Name the blood parasite species.
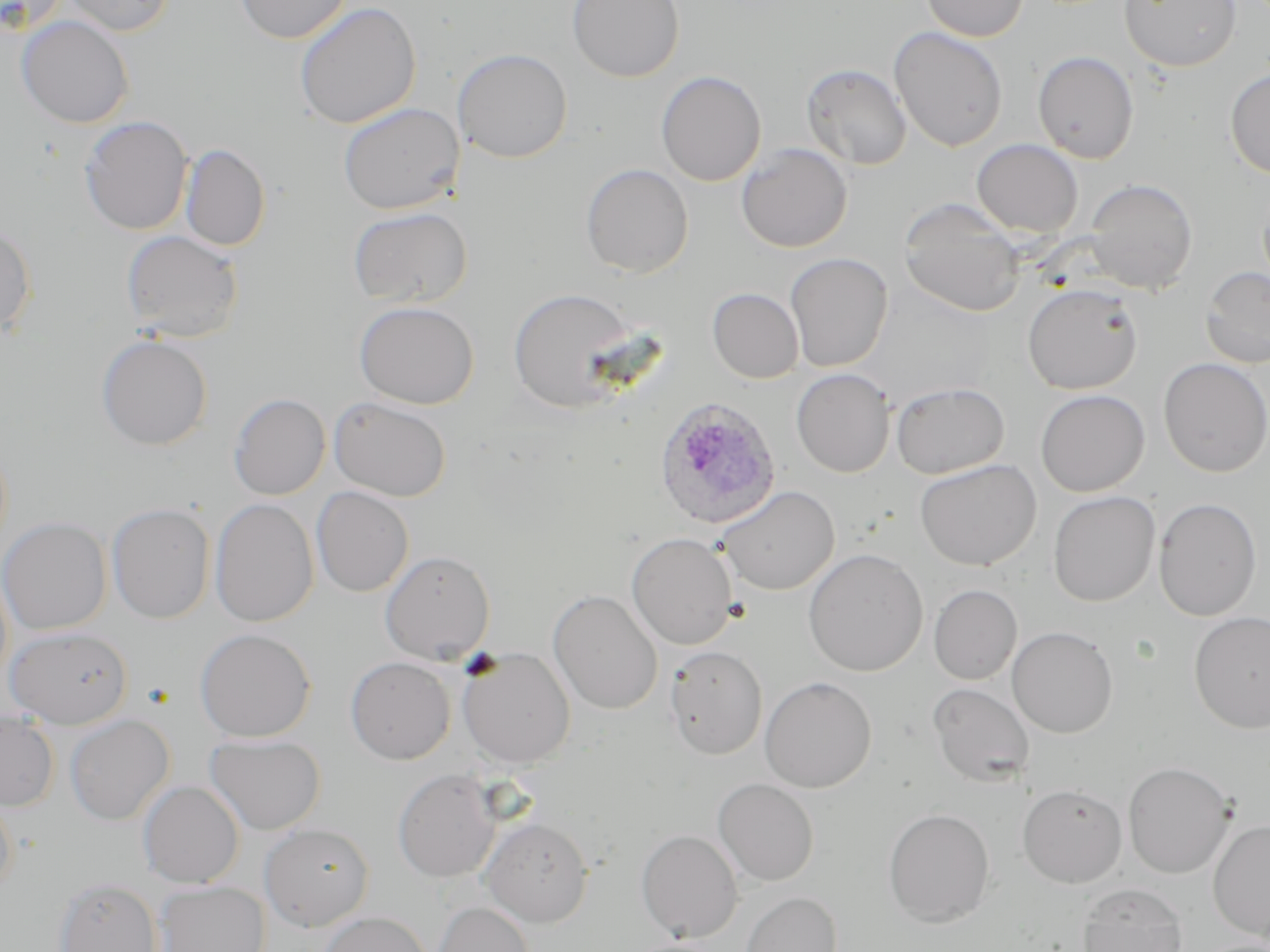

Plasmodium ovale.

Approximate bounding boxes as named x1/y1/x2/y2 corners in pixels. Uninfected red blood cell locations: (x1=3, y1=0, x2=71, y2=35), (x1=60, y1=0, x2=174, y2=36), (x1=234, y1=0, x2=352, y2=44), (x1=567, y1=0, x2=684, y2=82), (x1=921, y1=0, x2=1030, y2=41), (x1=1119, y1=0, x2=1242, y2=72), (x1=294, y1=1, x2=421, y2=130), (x1=16, y1=15, x2=135, y2=129), (x1=889, y1=26, x2=1009, y2=152), (x1=453, y1=48, x2=572, y2=163), (x1=1033, y1=51, x2=1139, y2=164), (x1=801, y1=63, x2=912, y2=171), (x1=1225, y1=68, x2=1270, y2=179), (x1=656, y1=70, x2=766, y2=186), (x1=338, y1=102, x2=462, y2=214), (x1=80, y1=116, x2=193, y2=235), (x1=971, y1=139, x2=1084, y2=238), (x1=736, y1=143, x2=853, y2=253), (x1=180, y1=144, x2=270, y2=251), (x1=580, y1=163, x2=693, y2=278), (x1=1084, y1=178, x2=1198, y2=293), (x1=898, y1=199, x2=1025, y2=316), (x1=348, y1=206, x2=472, y2=308), (x1=0, y1=221, x2=37, y2=336), (x1=121, y1=230, x2=244, y2=343), (x1=785, y1=253, x2=893, y2=372), (x1=1200, y1=266, x2=1270, y2=369), (x1=1022, y1=283, x2=1143, y2=394), (x1=508, y1=288, x2=637, y2=414), (x1=707, y1=288, x2=804, y2=383), (x1=354, y1=300, x2=479, y2=409), (x1=96, y1=335, x2=213, y2=450), (x1=1158, y1=358, x2=1270, y2=477), (x1=791, y1=368, x2=895, y2=477), (x1=890, y1=381, x2=1010, y2=479), (x1=1036, y1=389, x2=1149, y2=496), (x1=229, y1=393, x2=330, y2=500), (x1=329, y1=397, x2=452, y2=501), (x1=914, y1=458, x2=1042, y2=571), (x1=310, y1=486, x2=414, y2=597), (x1=718, y1=486, x2=840, y2=595), (x1=1048, y1=491, x2=1160, y2=607), (x1=1153, y1=497, x2=1262, y2=621), (x1=210, y1=498, x2=319, y2=627), (x1=107, y1=503, x2=215, y2=624), (x1=0, y1=518, x2=112, y2=634), (x1=626, y1=532, x2=738, y2=649), (x1=803, y1=548, x2=928, y2=676), (x1=380, y1=550, x2=495, y2=664), (x1=929, y1=584, x2=1022, y2=685), (x1=548, y1=590, x2=663, y2=714), (x1=1189, y1=611, x2=1270, y2=733), (x1=1007, y1=626, x2=1118, y2=738), (x1=4, y1=627, x2=133, y2=728), (x1=195, y1=628, x2=316, y2=742), (x1=664, y1=645, x2=768, y2=759), (x1=457, y1=647, x2=575, y2=768), (x1=345, y1=656, x2=456, y2=764), (x1=760, y1=676, x2=878, y2=793), (x1=927, y1=682, x2=1036, y2=787), (x1=0, y1=712, x2=59, y2=810), (x1=65, y1=715, x2=174, y2=825), (x1=205, y1=734, x2=325, y2=834), (x1=1123, y1=761, x2=1236, y2=879), (x1=393, y1=769, x2=501, y2=883), (x1=713, y1=778, x2=819, y2=886), (x1=138, y1=781, x2=244, y2=888), (x1=1018, y1=784, x2=1127, y2=887), (x1=0, y1=790, x2=17, y2=899), (x1=883, y1=808, x2=995, y2=927), (x1=481, y1=817, x2=593, y2=926), (x1=1208, y1=819, x2=1270, y2=941), (x1=259, y1=823, x2=374, y2=931), (x1=636, y1=829, x2=742, y2=942), (x1=54, y1=877, x2=163, y2=952), (x1=156, y1=881, x2=270, y2=952), (x1=1077, y1=883, x2=1188, y2=952), (x1=740, y1=891, x2=842, y2=952), (x1=432, y1=900, x2=534, y2=952), (x1=318, y1=911, x2=431, y2=952). Plasmodium ovale-infected red blood cell locations: (x1=653, y1=397, x2=781, y2=528). Thin blood film. Single field of view. May-Grünwald-Giemsa-stained preparation. Light microscopy. 1000x magnification. Image is 1270×952 pixels.